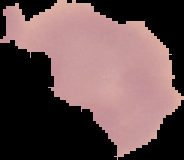

Summary:
  - Image type: segmented cell region on a black background
  - Preparation: thin blood film
  - Image size: 184×160 pixels
  - Malaria status: uninfected